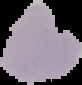

image size = 82×85 pixels
image type = segmented cell region with the area outside set to black
preparation = thin blood smear
malaria status = uninfected